Locate and identify every blood parasite.
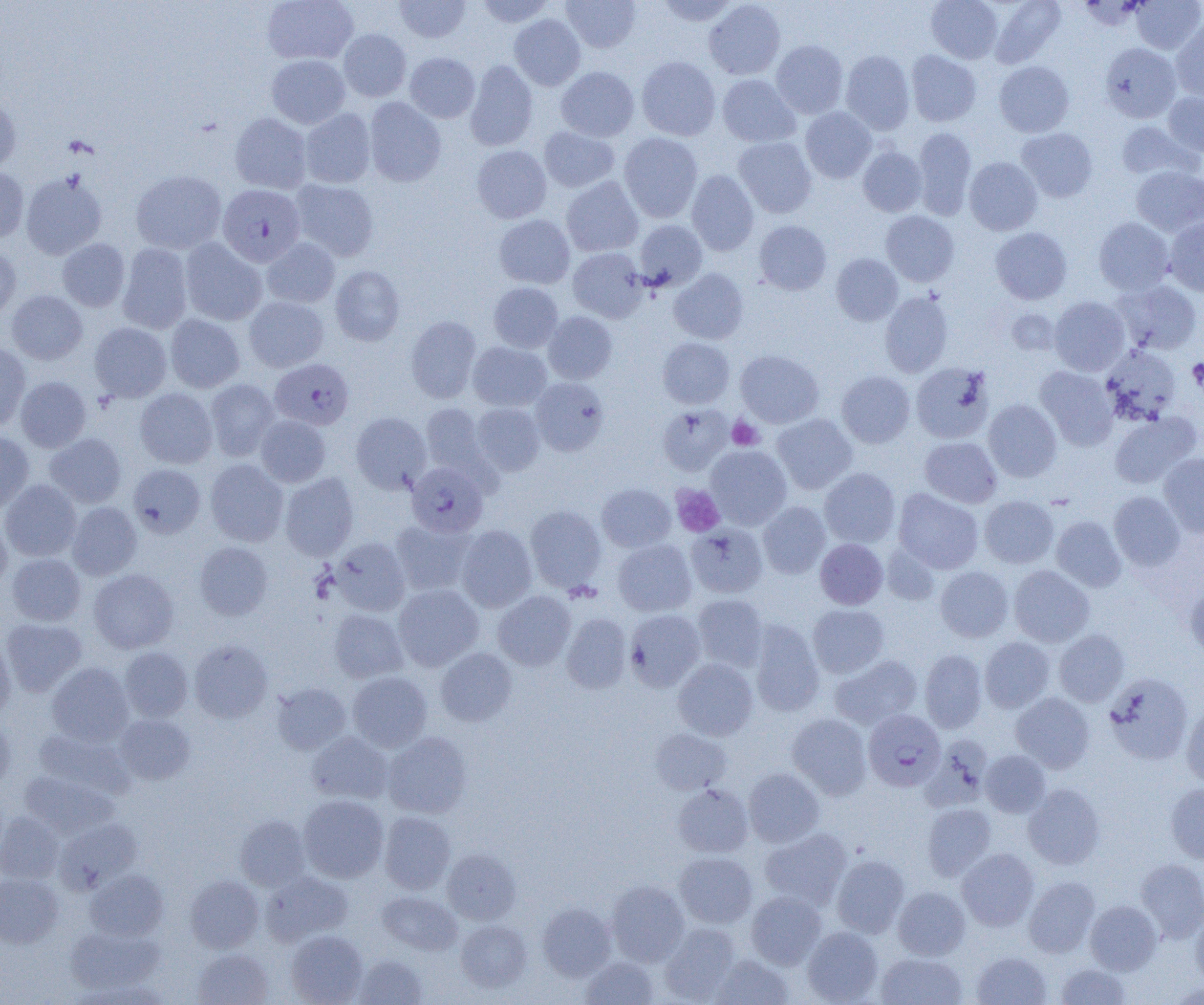
Approximate bounding boxes as [x1, y1, x2, y2] in pixels.
Plasmodium falciparum-infected red blood cells (subset): [218, 184, 305, 267], [270, 358, 354, 430], [407, 462, 488, 537], [863, 709, 945, 791].
No Plasmodium ovale, Plasmodium malariae, Plasmodium vivax, Babesia divergens, or Trypanosoma brucei observed.

Summary:
  - Uninfected red blood cell locations (subset): [262, 0, 358, 65], [395, 0, 470, 43], [476, 0, 554, 27], [562, 0, 640, 52], [656, 0, 739, 26], [926, 0, 1004, 63], [989, 0, 1066, 67], [1132, 0, 1203, 54], [704, 1, 785, 80], [509, 14, 585, 91], [1171, 22, 1204, 101], [339, 29, 411, 101], [771, 40, 848, 118], [1100, 43, 1180, 122], [840, 50, 914, 134], [906, 50, 981, 126], [405, 52, 480, 122], [267, 54, 350, 128], [636, 56, 721, 140], [465, 60, 538, 151], [994, 61, 1074, 137], [556, 66, 639, 141], [718, 74, 800, 147], [0, 92, 21, 173], [1163, 92, 1204, 156], [364, 97, 446, 186], [801, 107, 876, 182], [300, 109, 376, 188], [230, 112, 312, 193], [1116, 121, 1200, 181], [538, 126, 619, 192], [912, 127, 976, 220], [1016, 127, 1098, 202], [619, 133, 703, 222], [733, 137, 816, 218], [472, 145, 551, 223], [858, 146, 927, 216], [964, 157, 1042, 235], [1131, 165, 1204, 237], [0, 166, 29, 242], [686, 169, 759, 255], [131, 170, 226, 254], [21, 171, 107, 259], [562, 176, 643, 257], [290, 179, 379, 261], [881, 211, 959, 286], [494, 214, 574, 289], [1164, 216, 1204, 296], [1094, 217, 1174, 295], [635, 220, 707, 290], [754, 220, 831, 295], [990, 227, 1072, 304], [57, 238, 130, 312], [180, 238, 267, 325], [262, 238, 339, 308], [0, 244, 21, 321], [117, 244, 193, 334], [568, 247, 647, 322], [831, 253, 903, 325], [330, 265, 405, 346], [669, 268, 748, 344], [1114, 279, 1202, 355], [488, 282, 563, 353], [7, 290, 87, 364], [880, 292, 953, 377], [244, 296, 328, 372], [1049, 296, 1130, 376], [1006, 309, 1060, 355], [543, 311, 618, 384], [165, 314, 245, 393], [406, 316, 482, 403], [90, 322, 171, 402], [658, 337, 734, 408], [468, 341, 551, 411], [0, 343, 31, 432], [1100, 345, 1181, 425], [735, 350, 824, 428], [911, 362, 995, 444], [1035, 365, 1118, 450], [837, 371, 915, 448], [16, 376, 91, 452], [530, 377, 609, 456], [205, 379, 279, 461], [135, 388, 217, 468], [983, 399, 1062, 482], [471, 403, 545, 476], [421, 404, 491, 480], [657, 404, 733, 476], [351, 412, 431, 494], [1109, 412, 1201, 489], [771, 414, 857, 494], [256, 415, 330, 487], [0, 432, 34, 513], [45, 433, 127, 507], [920, 437, 1002, 507], [705, 445, 792, 530], [1159, 453, 1204, 537], [205, 459, 288, 546], [128, 464, 205, 537], [819, 468, 900, 547], [280, 473, 359, 561], [0, 479, 81, 561], [597, 484, 675, 552], [894, 489, 983, 574], [1109, 491, 1185, 571], [980, 496, 1059, 568], [758, 501, 831, 579], [67, 502, 142, 579], [525, 505, 607, 592], [0, 514, 12, 592], [1051, 516, 1126, 592], [390, 519, 476, 596], [456, 525, 537, 612], [330, 537, 411, 616], [815, 538, 888, 609], [613, 539, 696, 616], [195, 542, 273, 621], [881, 543, 940, 606], [6, 554, 86, 625], [1009, 565, 1094, 647], [935, 566, 1013, 642], [88, 569, 179, 653], [1184, 580, 1204, 659], [393, 584, 483, 671], [493, 591, 575, 671], [692, 593, 768, 672], [808, 604, 889, 678], [329, 609, 408, 682], [625, 609, 705, 692], [561, 613, 632, 693], [2, 618, 86, 696], [750, 620, 824, 717], [1054, 630, 1129, 706], [0, 635, 16, 720], [980, 637, 1054, 712], [189, 639, 273, 723], [120, 647, 192, 721], [436, 647, 517, 726], [920, 649, 987, 733], [830, 655, 922, 729], [673, 658, 758, 740], [47, 662, 134, 746], [348, 671, 432, 752], [1104, 672, 1193, 765], [271, 682, 351, 755], [1011, 692, 1095, 773], [1181, 706, 1204, 787], [114, 713, 195, 785], [787, 713, 871, 799], [0, 714, 15, 794], [650, 728, 732, 795], [33, 729, 135, 800], [306, 732, 393, 804], [383, 732, 472, 818], [981, 750, 1050, 817], [743, 767, 824, 847], [19, 771, 119, 839], [672, 783, 753, 857], [1023, 783, 1105, 869], [1166, 783, 1204, 864], [298, 794, 388, 883], [922, 803, 996, 881], [379, 811, 456, 894], [0, 812, 64, 884], [235, 815, 311, 891], [55, 818, 142, 893], [759, 828, 851, 910], [442, 847, 521, 924], [957, 848, 1039, 930], [674, 852, 757, 928], [831, 855, 909, 938], [1136, 858, 1204, 941], [85, 868, 169, 940], [261, 871, 353, 945], [0, 874, 63, 948], [185, 875, 264, 953], [1024, 877, 1100, 957], [606, 880, 688, 966], [893, 886, 970, 960], [746, 891, 826, 969], [377, 892, 462, 955], [1085, 900, 1162, 974], [538, 903, 616, 981], [1191, 909, 1204, 988], [456, 919, 532, 992], [659, 923, 740, 1003], [65, 925, 164, 994], [802, 926, 883, 1004], [286, 930, 367, 1005], [193, 948, 274, 1005], [972, 951, 1052, 1005], [876, 953, 967, 1004], [354, 954, 427, 1005], [709, 954, 794, 1005], [580, 956, 660, 1004], [1055, 963, 1131, 1005], [68, 979, 171, 1004], [1166, 981, 1204, 1004]
  - Platelet locations: [1188, 356, 1204, 396], [727, 416, 763, 450], [671, 484, 724, 537]
  - Slide-level diagnosis: Plasmodium falciparum
  - Modality: light microscopy
  - Preparation: thin blood smear
  - Magnification: 1000x
  - Field of view: one of a larger specimen
  - Image size: 1204×1005 pixels